Name the parasite shown.
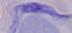

This is a trypanosome.

Captured at 1000x magnification. Photomicrograph.